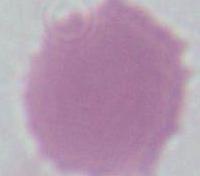

Summary:
  - Magnification: 1000x
  - Identification: red blood cell
  - Modality: photomicrograph